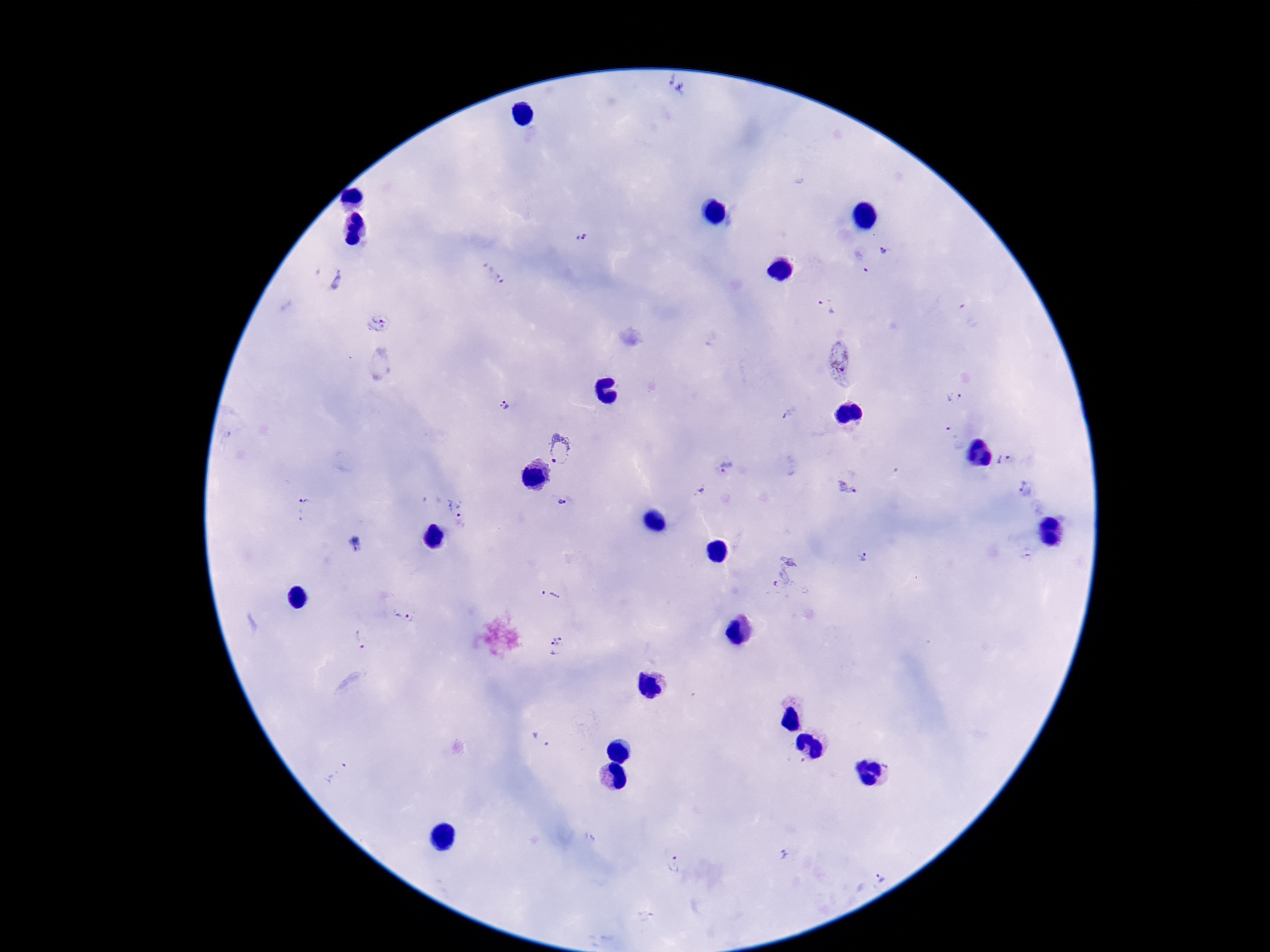
Approximate centers as (x, y) in pixels. Plasmodium parasite locations: (677, 85), (581, 237), (884, 253), (861, 262), (494, 273), (336, 280), (827, 307), (971, 314), (378, 325), (380, 363), (838, 363), (954, 397), (505, 405), (789, 414), (952, 433), (560, 449), (1004, 460), (725, 469), (848, 488), (1026, 488), (701, 493), (562, 502), (303, 508), (459, 509), (358, 545), (1028, 556), (866, 558), (787, 574), (552, 594), (405, 614), (359, 639), (557, 647), (541, 739), (340, 773), (784, 855), (674, 864), (881, 876). Giemsa-stained preparation. One field from this slide. Image is 1270×952 pixels. Smartphone photograph taken through the microscope eyepiece. Thick peripheral-blood smear. 100x magnification. Patient malaria status: infected.